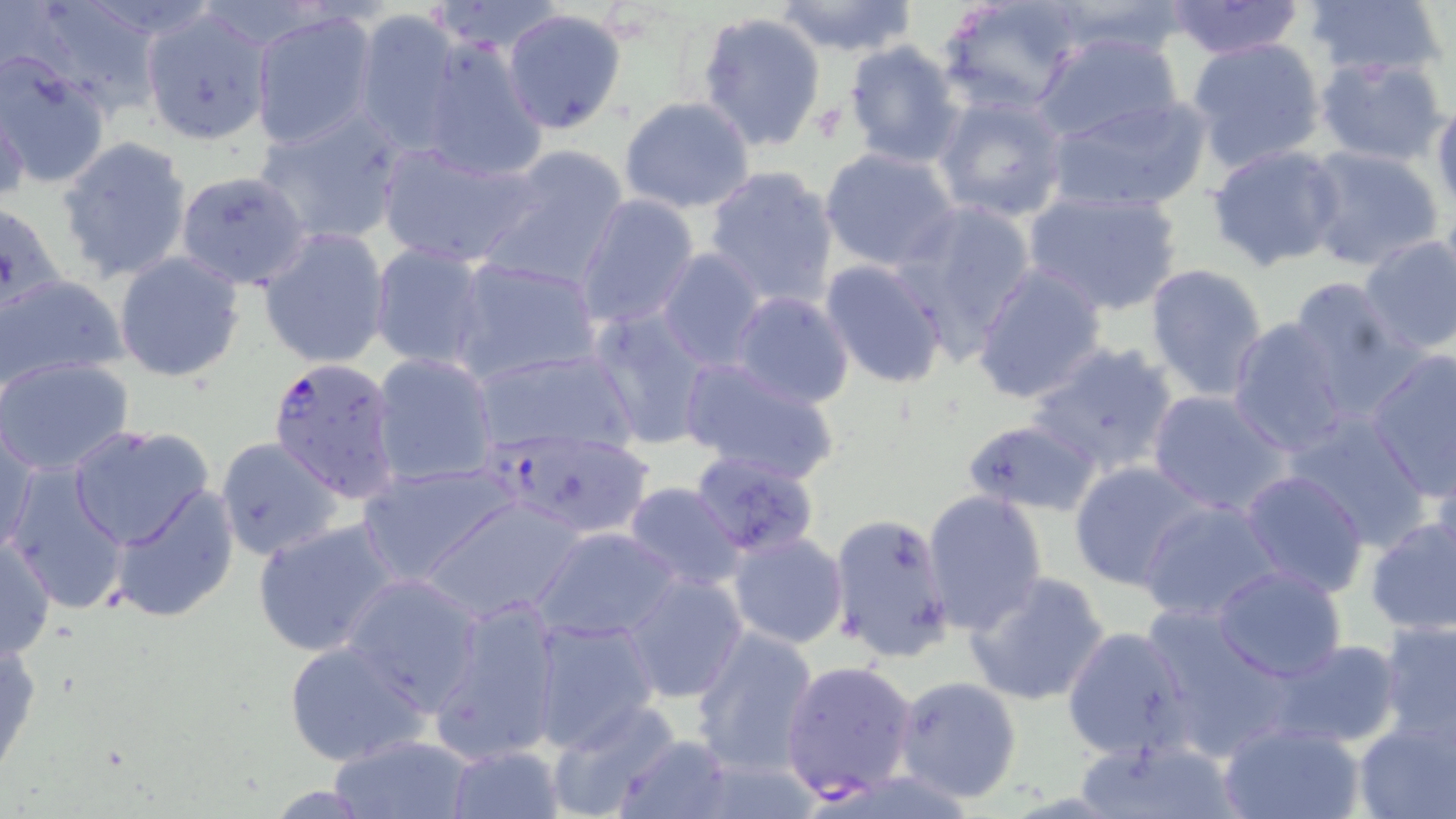 Approximate bounding boxes as [x1, y1, x2, y2] in pixels. Plasmodium falciparum-infected red blood cell locations: [267, 356, 402, 502], [485, 427, 656, 541], [779, 658, 919, 803]. Uninfected red blood cell locations: [11, 0, 159, 118], [425, 0, 568, 56], [937, 0, 1080, 116], [1042, 0, 1192, 62], [1304, 0, 1447, 80], [770, 1, 920, 56], [1161, 1, 1307, 60], [140, 9, 274, 144], [502, 9, 629, 134], [250, 10, 378, 149], [354, 10, 464, 154], [696, 10, 827, 154], [1032, 31, 1185, 149], [417, 35, 548, 181], [1187, 36, 1327, 171], [842, 40, 965, 169], [0, 52, 111, 190], [1314, 55, 1449, 165], [934, 94, 1069, 224], [1044, 94, 1214, 214], [617, 96, 756, 215], [1, 99, 29, 210], [1431, 100, 1456, 218], [254, 107, 406, 246], [58, 135, 194, 285], [376, 140, 541, 270], [1206, 143, 1345, 271], [475, 145, 630, 296], [1303, 145, 1442, 271], [819, 148, 961, 272], [703, 165, 839, 309], [176, 169, 312, 288], [1021, 185, 1185, 315], [575, 195, 702, 329], [0, 197, 69, 311], [890, 200, 1037, 362], [255, 226, 392, 371], [1356, 234, 1456, 357], [368, 243, 492, 372], [655, 249, 768, 369], [113, 253, 246, 383], [450, 256, 603, 387], [819, 258, 949, 390], [1143, 262, 1271, 401], [973, 263, 1109, 405], [0, 272, 128, 391], [1285, 276, 1412, 410], [729, 290, 855, 409], [587, 307, 719, 451], [1227, 317, 1353, 455], [1026, 341, 1183, 480], [468, 345, 642, 459], [1364, 348, 1454, 498], [369, 352, 498, 488], [1, 356, 135, 476], [678, 356, 842, 484], [1146, 388, 1293, 516], [1280, 410, 1435, 551], [961, 418, 1102, 516], [1, 424, 40, 558], [67, 424, 216, 551], [0, 435, 64, 588], [214, 436, 344, 562], [1427, 447, 1456, 570], [1068, 461, 1212, 591], [358, 462, 517, 585], [6, 464, 133, 615], [1239, 470, 1369, 597], [622, 483, 746, 595], [110, 485, 239, 622], [922, 491, 1049, 635], [421, 494, 591, 624], [1134, 497, 1286, 625], [828, 511, 954, 664], [252, 517, 402, 657], [1362, 517, 1456, 637], [532, 526, 682, 643], [726, 532, 849, 649], [0, 538, 55, 661], [1210, 564, 1349, 682], [963, 570, 1111, 708], [341, 573, 483, 714], [619, 573, 750, 704], [430, 596, 563, 765], [1152, 608, 1299, 758], [528, 614, 659, 752], [1377, 618, 1456, 745], [1062, 624, 1194, 760], [690, 626, 821, 775], [0, 635, 44, 783], [284, 639, 429, 767], [1266, 639, 1401, 749], [894, 675, 1023, 802], [545, 701, 684, 819], [1353, 711, 1455, 819], [1219, 720, 1365, 819], [330, 734, 473, 817], [610, 735, 736, 819], [1070, 735, 1246, 819], [442, 743, 565, 818]. Slide-level diagnosis: Plasmodium falciparum. Single field of view. Captured at 1000x magnification. Image is 1456×819 pixels. Thin blood film. Optical microscopy. May-Grünwald-Giemsa-stained preparation.